Locate platelets.
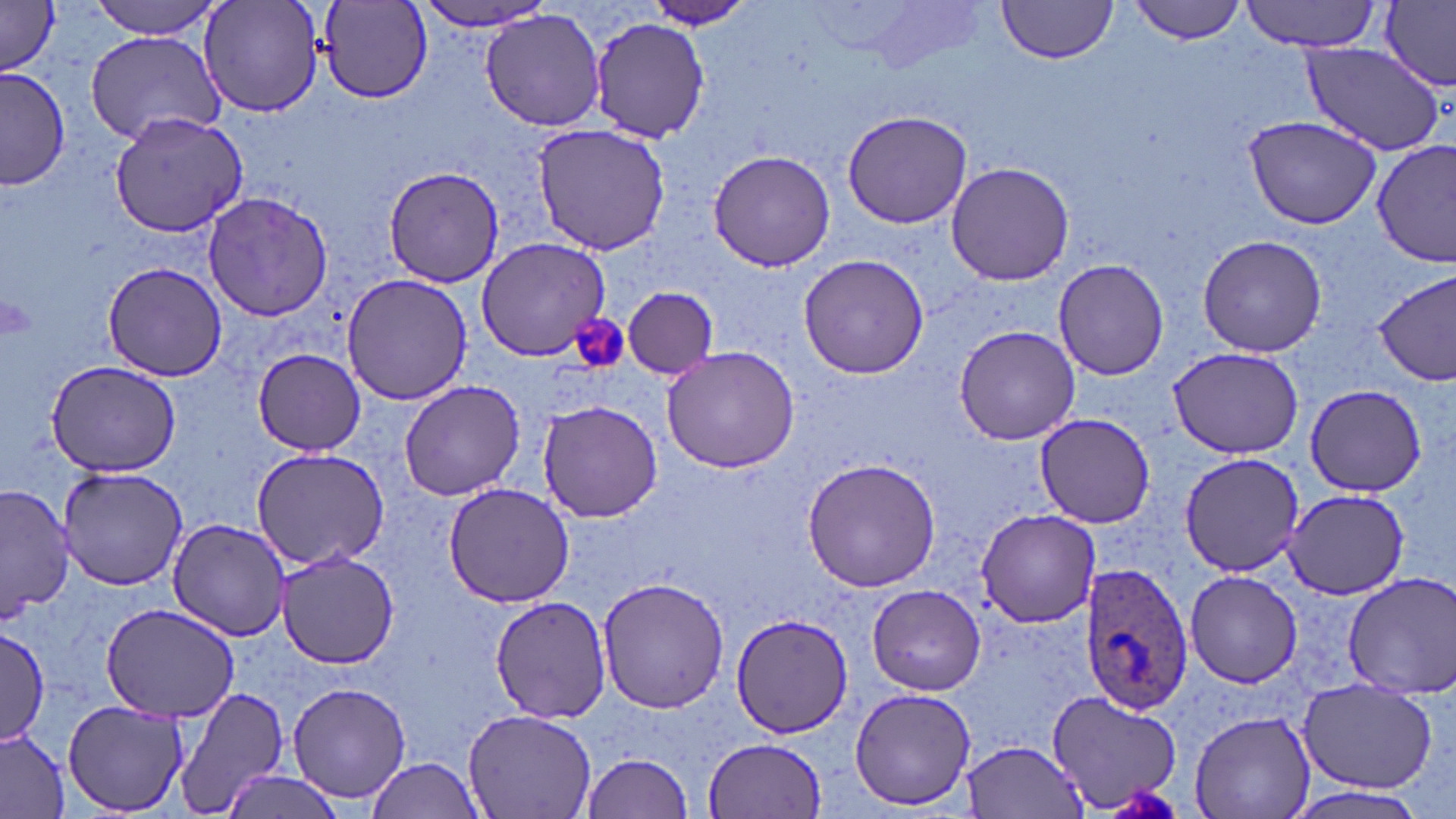
Approximate bounding boxes as named x1/y1/x2/y2 corners in pixels.
Platelets: (x1=570, y1=317, x2=628, y2=374).

Uninfected red blood cell locations: (x1=88, y1=0, x2=230, y2=39), (x1=198, y1=0, x2=325, y2=120), (x1=645, y1=0, x2=753, y2=31), (x1=1129, y1=0, x2=1247, y2=44), (x1=1241, y1=0, x2=1385, y2=51), (x1=1380, y1=0, x2=1456, y2=91), (x1=317, y1=1, x2=431, y2=103), (x1=415, y1=1, x2=558, y2=33), (x1=994, y1=1, x2=1117, y2=66), (x1=1, y1=3, x2=62, y2=74), (x1=482, y1=8, x2=606, y2=131), (x1=588, y1=17, x2=710, y2=141), (x1=85, y1=30, x2=226, y2=145), (x1=1299, y1=41, x2=1446, y2=156), (x1=0, y1=65, x2=70, y2=193), (x1=842, y1=109, x2=973, y2=230), (x1=107, y1=110, x2=248, y2=240), (x1=1245, y1=115, x2=1382, y2=229), (x1=530, y1=122, x2=670, y2=256), (x1=1373, y1=139, x2=1454, y2=267), (x1=707, y1=150, x2=838, y2=272), (x1=945, y1=161, x2=1075, y2=285), (x1=380, y1=166, x2=504, y2=287), (x1=201, y1=190, x2=335, y2=320), (x1=1196, y1=233, x2=1327, y2=357), (x1=474, y1=237, x2=609, y2=360), (x1=797, y1=251, x2=933, y2=378), (x1=1053, y1=259, x2=1170, y2=381), (x1=102, y1=261, x2=230, y2=383), (x1=1374, y1=269, x2=1456, y2=387), (x1=341, y1=274, x2=475, y2=405), (x1=622, y1=287, x2=718, y2=377), (x1=954, y1=324, x2=1080, y2=446), (x1=661, y1=344, x2=803, y2=472), (x1=1166, y1=346, x2=1305, y2=458), (x1=252, y1=348, x2=368, y2=456), (x1=46, y1=358, x2=184, y2=477), (x1=398, y1=379, x2=525, y2=500), (x1=1305, y1=384, x2=1428, y2=497), (x1=538, y1=400, x2=662, y2=523), (x1=1033, y1=413, x2=1158, y2=528), (x1=251, y1=447, x2=391, y2=571), (x1=1176, y1=453, x2=1307, y2=575), (x1=802, y1=456, x2=943, y2=593), (x1=56, y1=464, x2=189, y2=591), (x1=442, y1=482, x2=578, y2=607), (x1=1, y1=484, x2=75, y2=622), (x1=1283, y1=487, x2=1407, y2=600), (x1=976, y1=508, x2=1101, y2=626), (x1=168, y1=517, x2=292, y2=641), (x1=276, y1=550, x2=402, y2=669), (x1=1184, y1=569, x2=1303, y2=689), (x1=1339, y1=572, x2=1456, y2=698), (x1=596, y1=578, x2=730, y2=713), (x1=866, y1=585, x2=986, y2=694), (x1=490, y1=594, x2=614, y2=723), (x1=99, y1=602, x2=242, y2=721), (x1=730, y1=611, x2=849, y2=738), (x1=0, y1=627, x2=51, y2=744), (x1=287, y1=681, x2=413, y2=804), (x1=167, y1=683, x2=288, y2=819), (x1=1299, y1=684, x2=1436, y2=792), (x1=850, y1=687, x2=977, y2=811), (x1=1046, y1=689, x2=1182, y2=813), (x1=62, y1=700, x2=188, y2=816), (x1=463, y1=706, x2=597, y2=819), (x1=1189, y1=709, x2=1316, y2=819), (x1=0, y1=728, x2=72, y2=818), (x1=703, y1=737, x2=827, y2=819), (x1=963, y1=740, x2=1089, y2=816), (x1=583, y1=752, x2=696, y2=818), (x1=363, y1=757, x2=485, y2=818), (x1=219, y1=770, x2=339, y2=819), (x1=1284, y1=784, x2=1434, y2=819). Plasmodium ovale-infected red blood cell locations: (x1=1082, y1=563, x2=1195, y2=713). Slide-level diagnosis: Plasmodium ovale. Optical microscopy. Thin blood film. Captured at 1000x magnification. One field of a larger specimen. Image is 1456×819 pixels. May-Grünwald-Giemsa stain.